Locate every white blood cell.
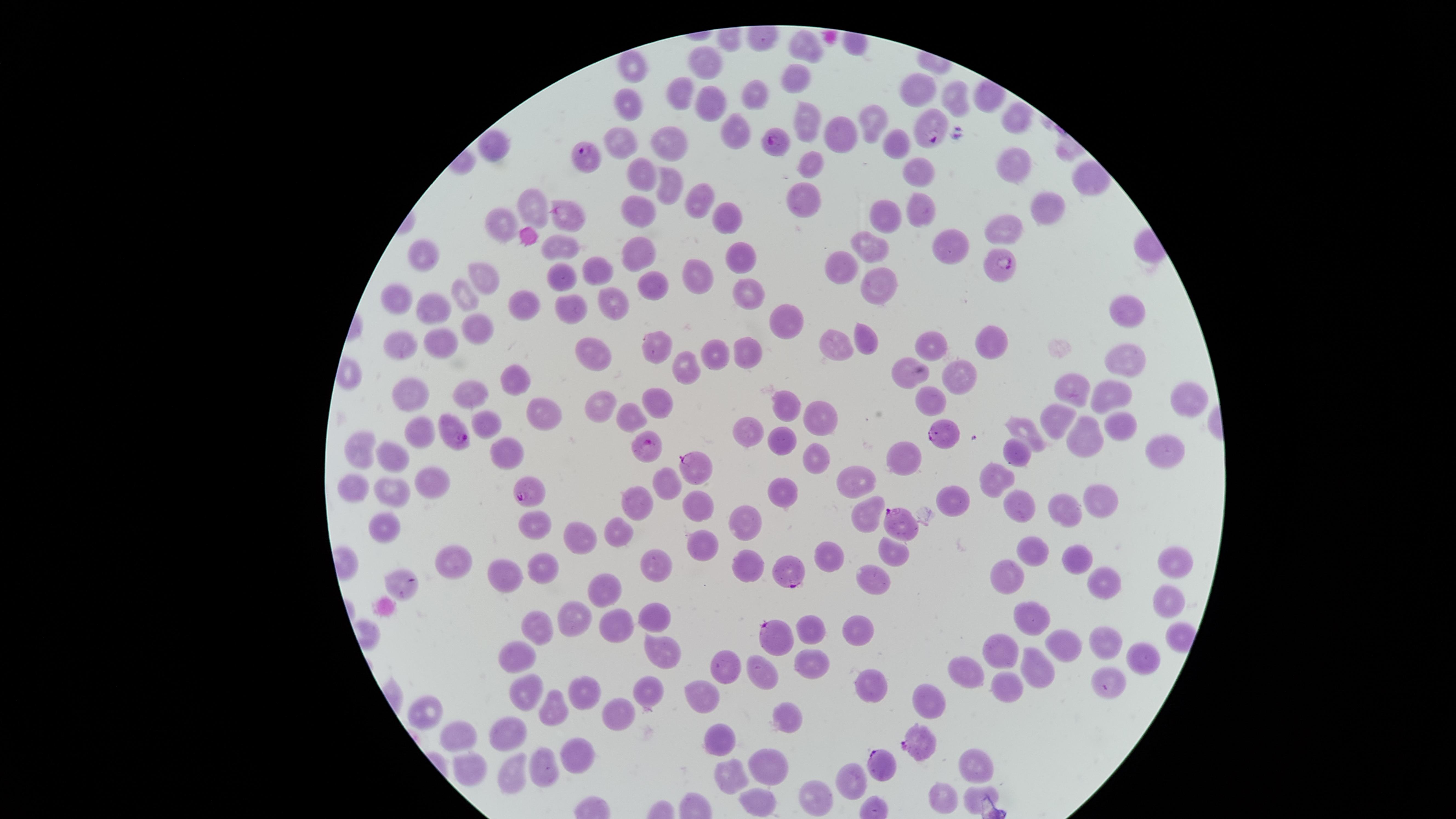
No white blood cells identified.

Approximate marker points as [x, y] in pixels. Uninfected red blood cells: [803, 44], [712, 61], [629, 68], [796, 81], [923, 89], [678, 92], [751, 94], [958, 99], [710, 100], [628, 110], [1018, 117], [871, 119], [807, 125], [736, 128], [840, 136], [671, 140], [624, 143], [495, 146], [902, 146], [1014, 161], [808, 164], [919, 170], [641, 175], [671, 184], [805, 191], [700, 197], [525, 201], [638, 206], [920, 207], [1042, 208], [888, 216], [720, 218], [493, 222], [1001, 228], [951, 244], [870, 246], [562, 248], [640, 249], [739, 254], [847, 256], [424, 262], [598, 268], [696, 274], [483, 277], [559, 280], [654, 284], [876, 284], [743, 290], [458, 293], [398, 299], [609, 299], [520, 302], [438, 306], [567, 309], [1125, 309], [783, 317], [476, 326], [441, 336], [655, 341], [403, 343], [865, 343], [932, 343], [833, 344], [986, 347], [603, 348], [749, 348], [710, 349], [1123, 359], [683, 365], [910, 370], [957, 373], [520, 377], [1077, 385], [416, 390], [473, 391], [1110, 393], [1183, 398], [932, 399], [654, 401], [791, 402], [602, 406], [546, 407], [629, 413], [821, 418], [1058, 419], [492, 422], [1119, 422], [417, 427], [745, 428], [1026, 430], [783, 436], [1083, 438], [1159, 443], [356, 445], [510, 454], [813, 454], [1016, 454], [904, 457], [399, 460], [993, 475], [856, 479], [433, 481], [666, 481], [357, 484], [391, 489], [775, 492], [951, 496], [695, 498], [1095, 498], [639, 501], [1016, 504], [1059, 508], [863, 516], [746, 522], [530, 530], [624, 531], [389, 533], [582, 534], [703, 542], [1041, 548], [892, 554], [660, 558], [1084, 558], [830, 559], [452, 561], [542, 565], [743, 565], [1170, 566], [510, 575], [1015, 576], [404, 580], [872, 582], [1107, 582], [608, 590], [1162, 600], [649, 618], [1026, 618], [576, 619], [816, 623], [856, 626], [618, 627], [531, 630], [1106, 637], [1063, 643], [1003, 648], [659, 649], [1146, 652], [515, 659], [813, 662], [723, 666], [972, 670], [1032, 672], [760, 673], [1104, 678], [873, 684], [525, 687], [588, 689], [648, 691], [1001, 692], [703, 695], [927, 699], [555, 704], [616, 715], [792, 719], [504, 732], [457, 735], [719, 736], [575, 751], [546, 761], [770, 761], [977, 766], [473, 768], [513, 772], [734, 773], [848, 778], [812, 794], [940, 796], [974, 796], [756, 798]. Parasitized red blood cells: [936, 128], [776, 143], [584, 153], [566, 215], [999, 262], [455, 430], [946, 431], [651, 445], [696, 466], [530, 491], [898, 519], [791, 568], [772, 634], [921, 743], [877, 764]. Photographed with a smartphone camera through the microscope eyepiece. Image is 1456×819 pixels. Species: Plasmodium falciparum. Single field of view. The visible region is circular. Presence: malaria parasites detected. Thin blood smear. Giemsa-stained preparation.